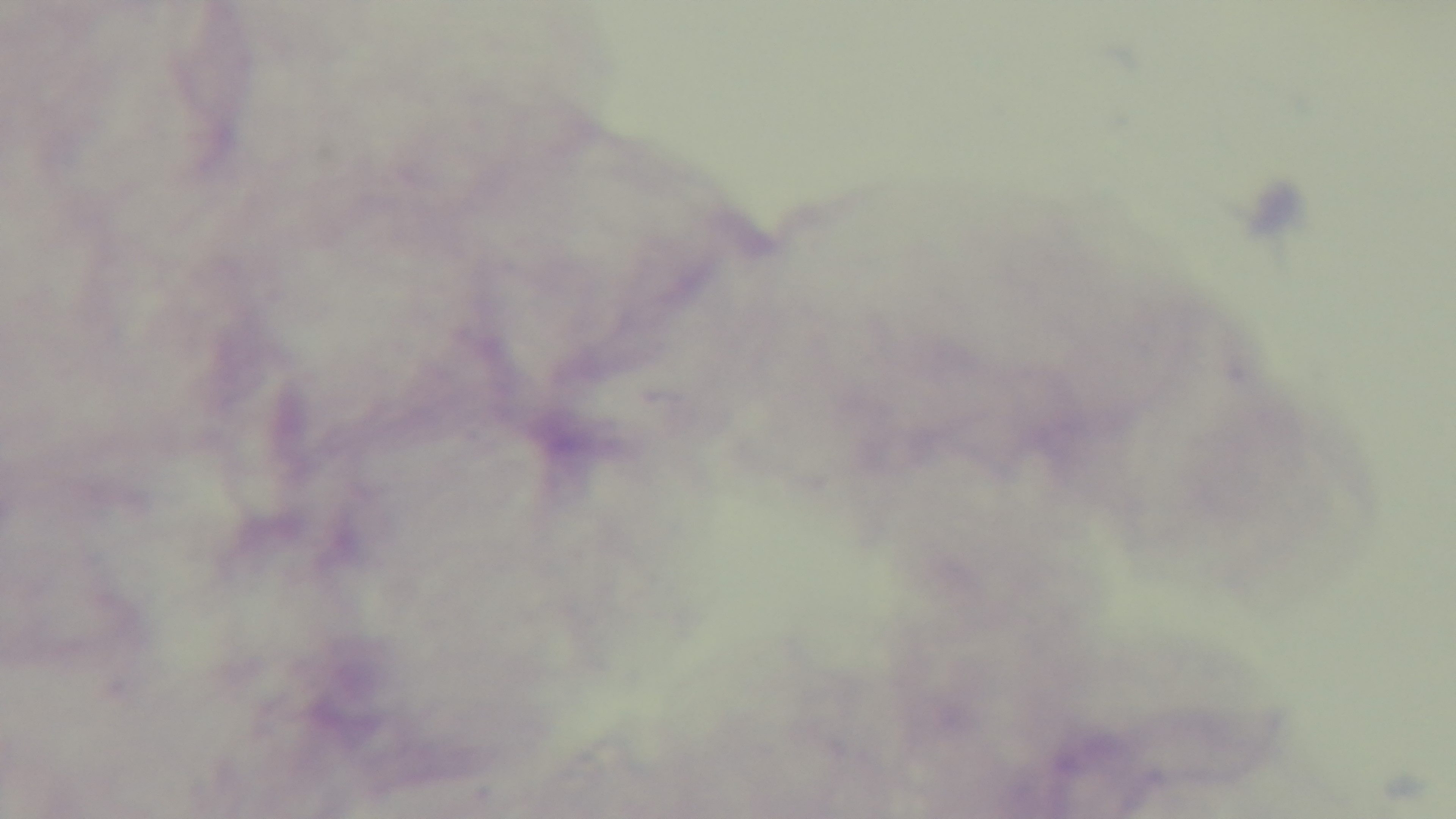

Preparation: thick smear. Oil-immersion objective, 100x. Malaria status: negative. Single field of view. Giemsa stain. Captured with a mounted 4K digital camera. Photomicrograph.